Classify this cell by malaria status.
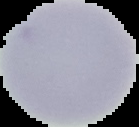
It is uninfected.

Segmented cell region on a black background. Image is 139×127 pixels. From a thin blood smear.